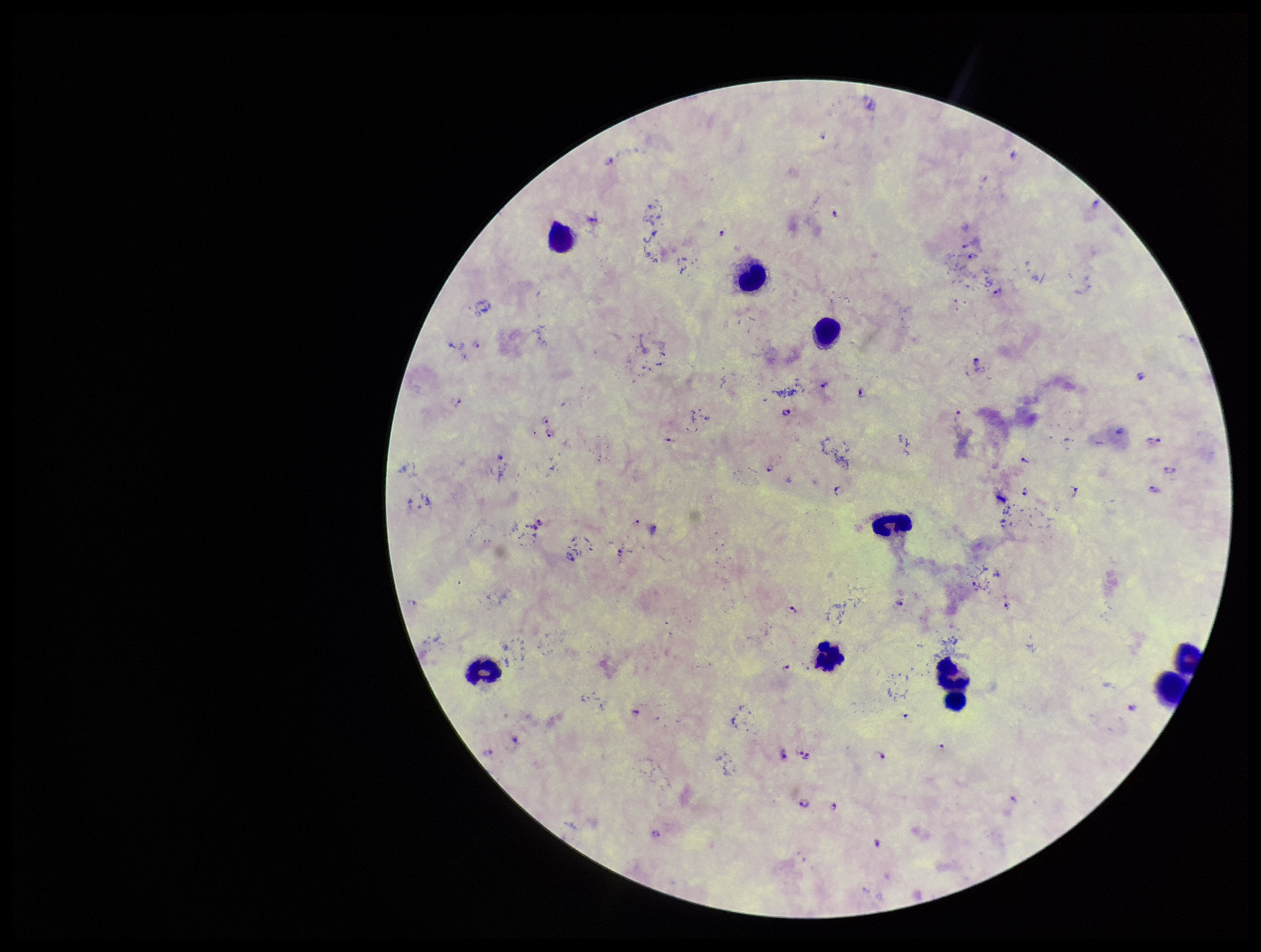
image size = 1261×952 pixels
preparation = thick
leukocyte count = 8
field of view = single
stain = Giemsa
capture = smartphone photograph through the microscope eyepiece
patient malaria status = infected
Plasmodium parasites = identified
parasite count = 42
species reported for this patient = Plasmodium falciparum